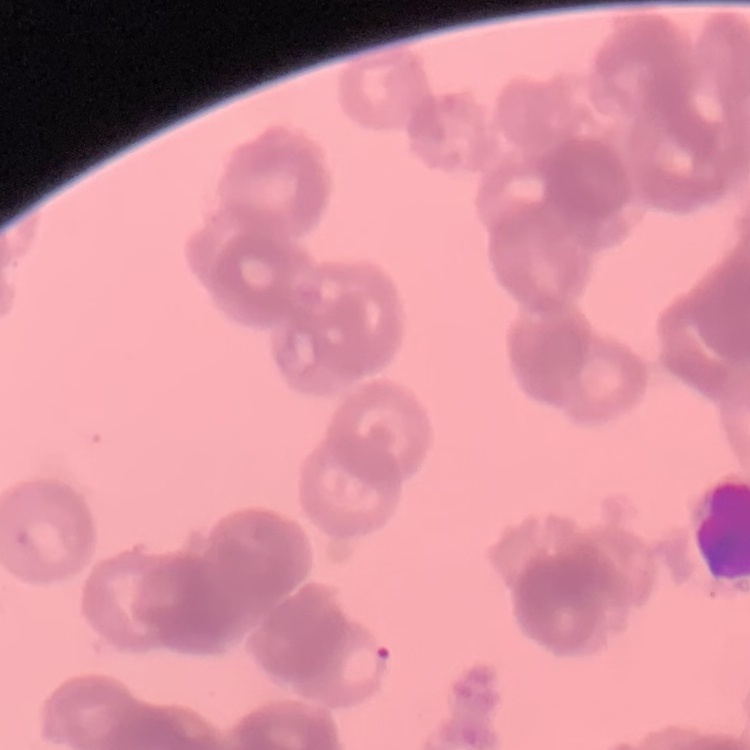

erythrocyte_morphology: rouleaux formation
preparation: thin blood smear
image_type: square crop of a larger photomicrograph
stain: Field's or Giemsa